Name the parasite shown.
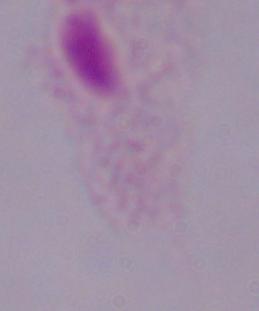
This is a trichomonad.

magnification: 1000x
modality: micrograph